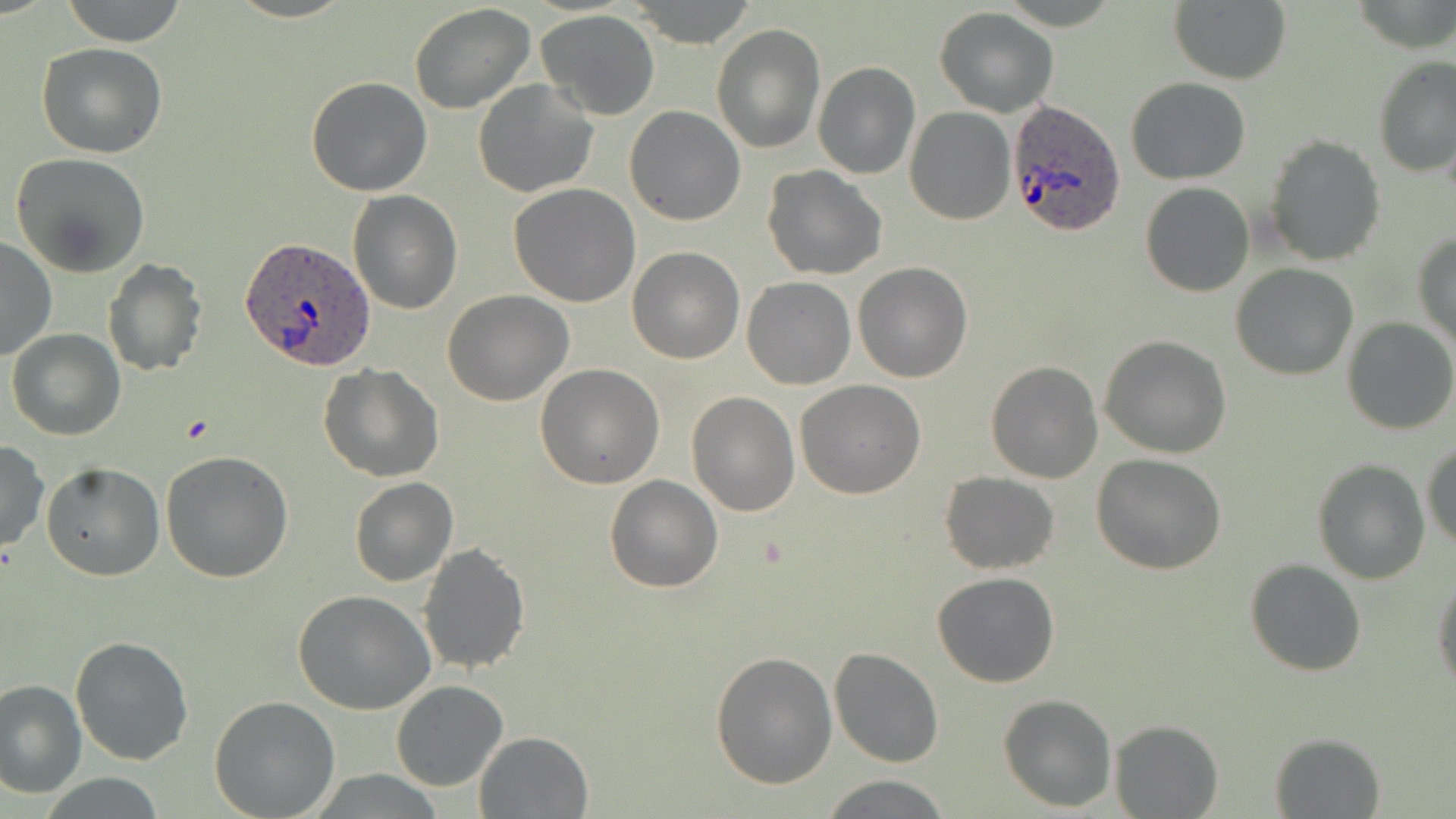 Approximate bounding boxes as (x1, y1, x2, y2) in pixels. Plasmodium ovale-infected red blood cell locations: (1006, 100, 1126, 235), (240, 238, 375, 373). Uninfected red blood cell locations: (61, 0, 187, 47), (1169, 0, 1291, 84), (626, 1, 757, 46), (408, 3, 536, 114), (934, 7, 1057, 116), (538, 10, 661, 121), (713, 24, 825, 153), (36, 43, 168, 159), (1373, 54, 1455, 182), (812, 63, 922, 181), (306, 76, 433, 196), (1127, 77, 1250, 184), (472, 79, 600, 200), (625, 105, 744, 224), (905, 107, 1015, 224), (1265, 135, 1385, 267), (10, 153, 153, 277), (762, 166, 887, 279), (1140, 181, 1254, 296), (508, 183, 641, 306), (349, 191, 462, 314), (1412, 229, 1456, 349), (0, 235, 57, 361), (627, 247, 745, 365), (102, 258, 206, 376), (853, 262, 973, 383), (1231, 264, 1359, 380), (741, 277, 855, 389), (442, 291, 573, 406), (1344, 317, 1456, 435), (7, 328, 125, 440), (1100, 335, 1232, 457), (986, 361, 1103, 483), (535, 363, 664, 489), (319, 364, 444, 482), (795, 381, 926, 499), (686, 391, 799, 515), (1423, 440, 1455, 551), (0, 441, 47, 553), (160, 449, 295, 582), (1092, 453, 1225, 574), (1312, 459, 1430, 585), (41, 463, 165, 582), (940, 471, 1060, 574), (604, 474, 723, 592), (350, 477, 457, 587), (417, 542, 531, 675), (1245, 558, 1365, 677), (1433, 571, 1455, 697), (931, 572, 1060, 688), (294, 592, 436, 715), (70, 636, 194, 766), (829, 647, 943, 767), (711, 649, 837, 789), (0, 680, 87, 800), (390, 680, 509, 791), (998, 693, 1116, 812), (209, 695, 340, 818), (1109, 719, 1223, 818), (474, 730, 592, 817), (1270, 732, 1384, 817), (820, 774, 951, 818), (39, 775, 167, 817). Slide-level diagnosis: Plasmodium ovale. Thin blood smear. Single field of view. 1000x magnification. Image is 1456×819 pixels. May-Grünwald-Giemsa stain. Light microscopy.